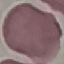
result: no malaria parasites detected
capture: smartphone camera at the microscope eyepiece
preparation: thin smear
image_type: automatically extracted cell patch, resized to 64 × 64 pixels
stain: Giemsa